Name the cell type shown.
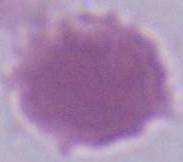
This is an erythrocyte.

Photomicrograph. 1000x magnification.